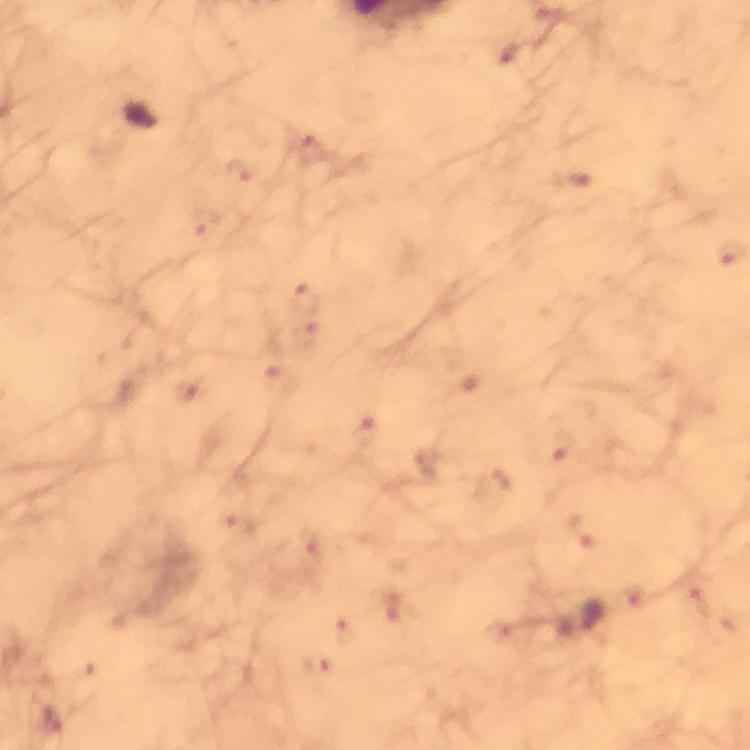

Approximate centers as (x, y) in pixels. Malaria parasite locations: (313, 152), (244, 170), (569, 182), (204, 225), (305, 295), (306, 337), (281, 378), (189, 393), (364, 434), (562, 441), (495, 480), (238, 526), (582, 531), (700, 602), (392, 604), (346, 629), (319, 665), (52, 725). From a malaria diagnostic workup. Immersion oil applied. At 100x magnification. Giemsa stain. A crop from one field of view. Image is 750×750 pixels. Thick blood smear. Photographed through the microscope with a smartphone camera.